Outline every malaria parasite.
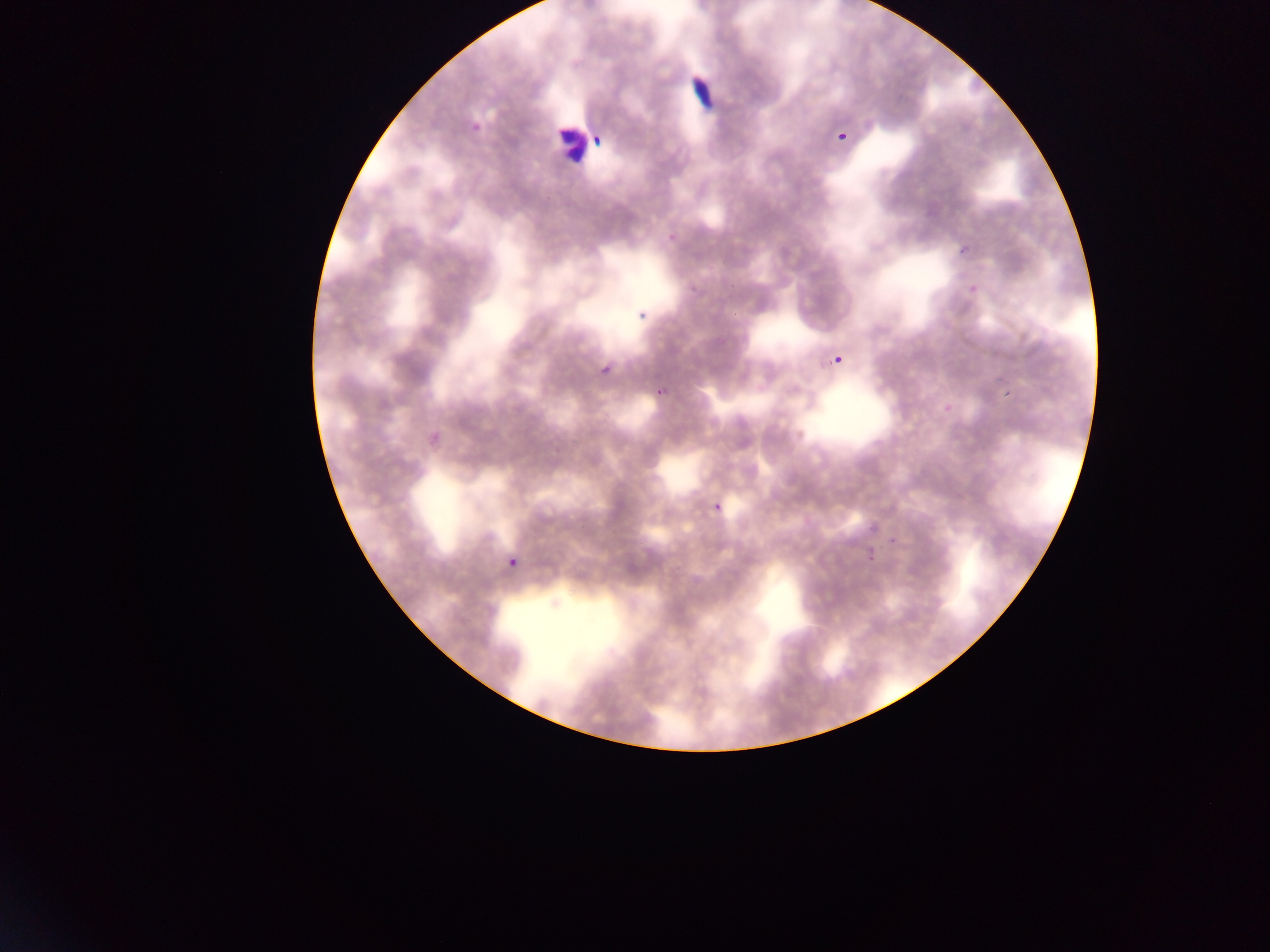

Approximate bounding boxes as {left, top, right, bottom} in pixels.
Malaria parasites (some below the resolvable threshold): {686, 72, 709, 113}, {561, 108, 585, 177}, {470, 121, 484, 136}, {837, 131, 851, 146}, {591, 134, 604, 148}, {630, 306, 645, 327}, {834, 352, 851, 372}, {599, 361, 617, 382}, {651, 385, 671, 408}, {707, 494, 733, 523}, {506, 554, 524, 576}.

Mobile-phone photograph taken through the microscope. Image is 1270×952 pixels. Collected in Ghana. One field of view. Thin blood film.